Classify this cell by malaria status.
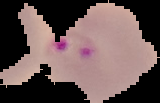

It is parasitized.

From a thin blood smear. Image is 160×103 pixels. Cell region segmented out of the field of view; the surrounding area is masked to black.